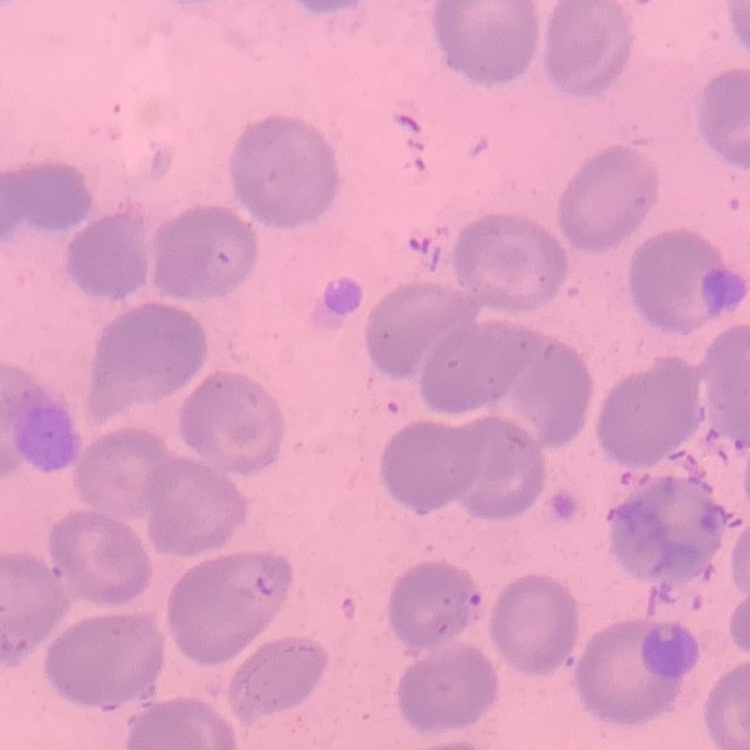

Summary:
  - Erythrocyte morphology: no rouleaux formation
  - Stain: Field's or Giemsa
  - Image type: square crop of a larger photomicrograph
  - Preparation: thin blood smear